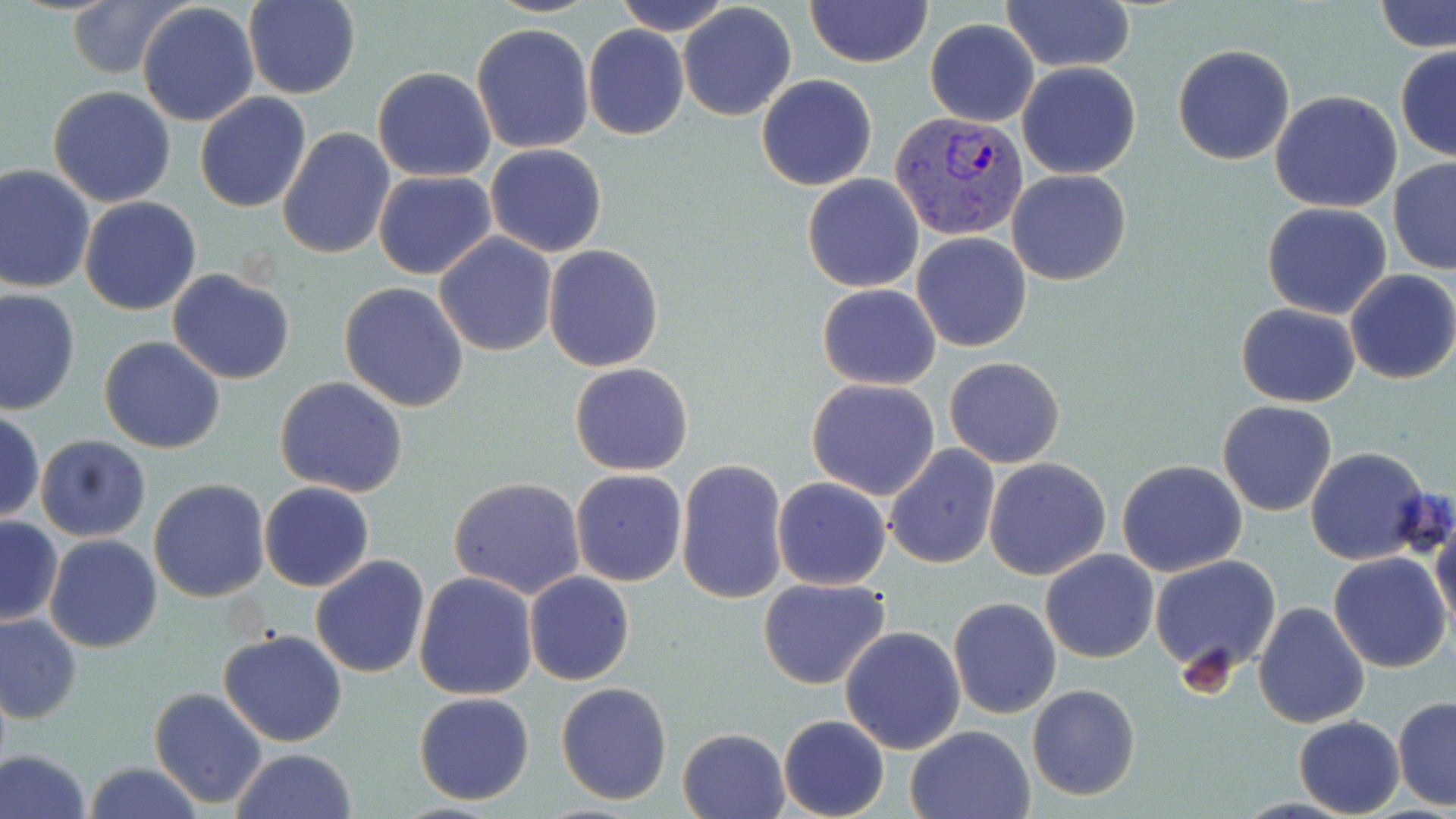
slide-level diagnosis = Plasmodium vivax
field of view = one of a larger specimen
Plasmodium vivax-infected red blood cell locations = approximate bounding boxes as (x1, y1, x2, y2) in pixels: (891, 109, 1027, 240)
stain = May-Grünwald-Giemsa
magnification = 1000x
modality = optical microscopy
uninfected red blood cell locations = approximate bounding boxes as (x1, y1, x2, y2) in pixels: (612, 0, 735, 35), (804, 0, 933, 68), (1377, 0, 1456, 54), (66, 1, 183, 80), (244, 1, 360, 100), (1004, 1, 1133, 74), (137, 2, 260, 128), (677, 4, 797, 120), (925, 19, 1039, 126), (471, 22, 594, 154), (583, 24, 689, 139), (1172, 43, 1296, 165), (1394, 47, 1456, 161), (1016, 61, 1141, 180), (372, 66, 497, 181), (756, 73, 878, 191), (47, 85, 178, 208), (1270, 90, 1402, 212), (195, 91, 311, 213), (277, 127, 396, 261), (484, 144, 609, 257), (1388, 158, 1456, 274), (0, 164, 95, 296), (372, 169, 496, 280), (1006, 169, 1131, 284), (803, 174, 924, 291), (79, 195, 202, 316), (1261, 203, 1392, 319), (433, 232, 559, 357), (912, 232, 1031, 351), (543, 244, 666, 372), (1342, 269, 1456, 384), (169, 270, 294, 385), (339, 282, 471, 412), (817, 283, 942, 389), (0, 288, 81, 417), (1235, 303, 1360, 407), (99, 336, 225, 455), (945, 356, 1065, 467), (569, 362, 693, 476), (274, 376, 408, 498), (806, 377, 943, 500), (1217, 401, 1338, 517), (1, 410, 45, 523), (35, 434, 153, 542), (884, 443, 999, 568), (1306, 447, 1433, 566), (984, 457, 1111, 581), (675, 458, 789, 605), (1116, 459, 1248, 577), (571, 469, 687, 585), (773, 476, 891, 590), (448, 477, 586, 599), (149, 479, 272, 603), (259, 481, 375, 593), (1428, 507, 1456, 639), (1, 516, 64, 627), (44, 534, 162, 655), (1040, 549, 1159, 663), (1328, 553, 1452, 674), (310, 555, 430, 678), (1149, 555, 1281, 675), (413, 571, 538, 700), (524, 571, 635, 686), (757, 576, 892, 688), (948, 598, 1062, 720), (1252, 600, 1372, 729), (0, 611, 82, 724), (840, 626, 966, 755), (217, 628, 349, 748), (556, 682, 673, 806), (1026, 685, 1140, 801), (149, 688, 267, 808), (412, 691, 536, 806), (1392, 696, 1456, 811), (777, 715, 889, 819), (1294, 716, 1404, 818), (905, 725, 1035, 818), (677, 727, 791, 819), (0, 747, 93, 819), (231, 748, 359, 819), (83, 763, 205, 819)
preparation = thin blood smear
image size = 1456×819 pixels